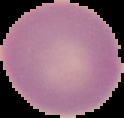

preparation = thin blood film
image size = 124×118 pixels
image type = segmented cell region with the area outside set to black
malaria status = uninfected